Outline each Plasmodium ovale-infected red blood cell.
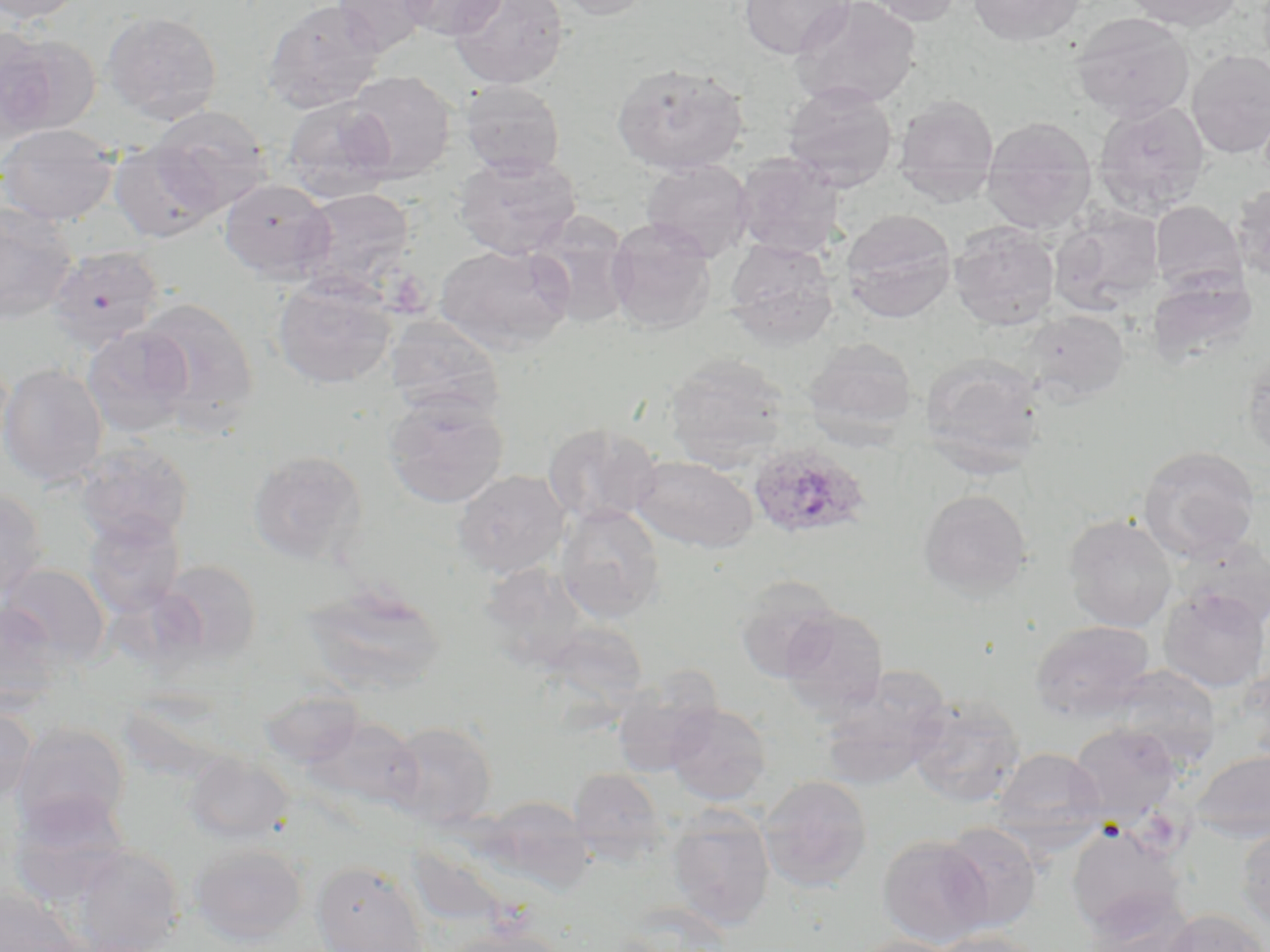
Approximate bounding boxes as [x1, y1, x2, y2] in pixels.
Plasmodium ovale-infected red blood cells: [747, 441, 873, 541].

Summary:
  - Uninfected red blood cell locations: [0, 0, 87, 25], [261, 0, 387, 114], [332, 0, 437, 56], [398, 0, 508, 40], [448, 0, 568, 89], [550, 0, 654, 21], [739, 0, 853, 59], [789, 0, 922, 110], [859, 0, 965, 27], [967, 0, 1086, 47], [1122, 0, 1244, 31], [101, 10, 223, 124], [1070, 11, 1195, 122], [0, 31, 97, 141], [1186, 49, 1270, 158], [612, 62, 747, 176], [344, 70, 456, 182], [459, 79, 565, 177], [781, 81, 898, 192], [893, 93, 999, 205], [281, 98, 397, 201], [1093, 99, 1211, 216], [149, 106, 271, 216], [981, 115, 1098, 233], [0, 123, 119, 226], [109, 140, 221, 242], [454, 152, 582, 259], [733, 152, 845, 258], [640, 158, 755, 261], [219, 178, 334, 282], [1231, 183, 1270, 283], [294, 187, 416, 297], [1150, 200, 1247, 294], [0, 203, 78, 325], [1050, 207, 1164, 316], [840, 210, 957, 323], [526, 213, 635, 331], [605, 218, 717, 335], [949, 223, 1060, 331], [724, 238, 838, 348], [434, 243, 574, 355], [46, 244, 165, 351], [1148, 272, 1257, 369], [271, 274, 398, 390], [136, 298, 259, 430], [1022, 310, 1130, 404], [383, 315, 505, 419], [80, 324, 195, 438], [803, 337, 917, 443], [1243, 350, 1270, 463], [665, 354, 789, 471], [921, 354, 1045, 478], [0, 362, 108, 488], [384, 393, 510, 509], [543, 422, 662, 526], [74, 441, 194, 548], [1138, 445, 1260, 562], [246, 449, 367, 567], [631, 454, 757, 553], [453, 469, 571, 578], [0, 486, 48, 602], [918, 488, 1032, 599], [556, 504, 665, 624], [83, 514, 186, 618], [1064, 514, 1178, 632], [1174, 538, 1270, 633], [152, 559, 263, 664], [1, 563, 111, 665], [733, 575, 842, 682], [302, 584, 447, 696], [1158, 586, 1269, 692], [0, 600, 65, 713], [779, 606, 889, 717], [1031, 620, 1155, 720], [541, 621, 649, 711], [1111, 665, 1221, 765], [818, 667, 952, 790], [610, 673, 722, 777], [259, 687, 366, 768], [908, 694, 1025, 808], [665, 701, 772, 806], [0, 703, 36, 807], [303, 713, 423, 812], [384, 720, 497, 828], [11, 722, 131, 835], [1067, 723, 1183, 822], [992, 747, 1106, 846], [1189, 748, 1270, 843], [182, 753, 292, 844], [569, 768, 667, 861], [759, 774, 873, 892], [8, 793, 133, 906], [480, 796, 594, 894], [667, 808, 775, 930], [937, 821, 1042, 933], [1067, 824, 1186, 938], [1236, 824, 1270, 931], [877, 834, 993, 948], [189, 842, 308, 944], [407, 843, 507, 931], [67, 845, 184, 952], [312, 860, 429, 952], [0, 888, 78, 952], [1086, 888, 1195, 952], [1159, 908, 1268, 952], [441, 927, 569, 952], [929, 930, 1046, 952], [849, 935, 967, 952]
  - Slide-level diagnosis: Plasmodium ovale
  - Field of view: single
  - Stain: May-Grünwald-Giemsa
  - Magnification: 1000x
  - Preparation: thin blood smear
  - Image size: 1270×952 pixels
  - Modality: optical microscopy